Assess this cell for malaria.
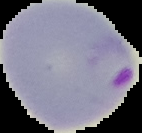
It is parasitized.

Summary:
  - Image size: 142×133 pixels
  - Image type: segmented cell region on a black background
  - Preparation: thin blood smear